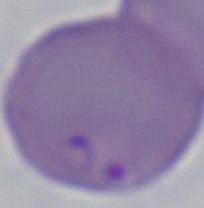
Micrograph. 1000x magnification. A Babesia parasite is seen.